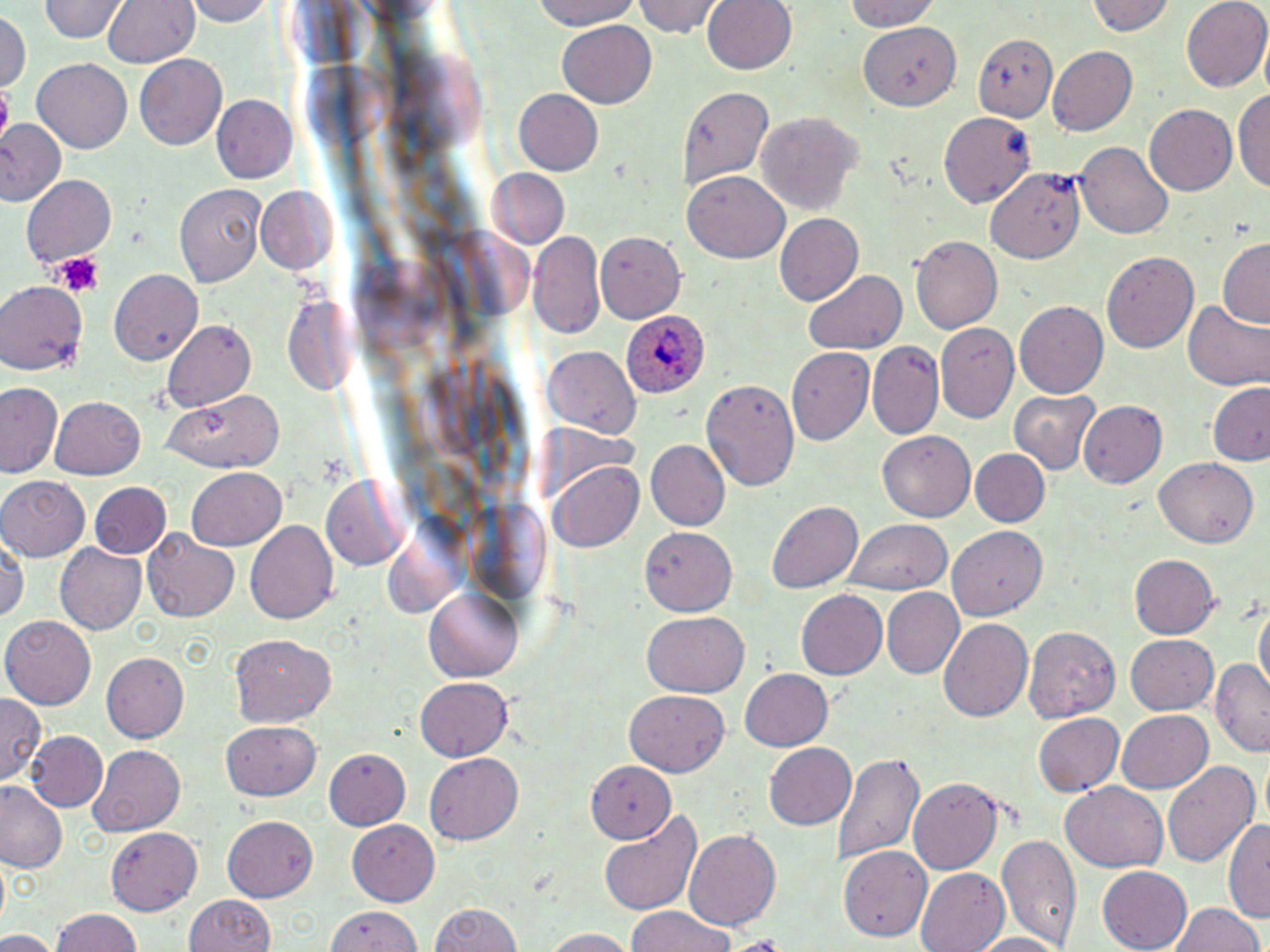

Summary:
  - Coordinate format: approximate bounding boxes as named x1/y1/x2/y2 corners in pixels
  - Platelet locations: (x1=0, y1=88, x2=12, y2=133), (x1=50, y1=252, x2=106, y2=298)
  - Uninfected red blood cell locations: (x1=40, y1=0, x2=127, y2=44), (x1=102, y1=0, x2=199, y2=70), (x1=188, y1=0, x2=274, y2=26), (x1=528, y1=0, x2=646, y2=29), (x1=634, y1=0, x2=725, y2=39), (x1=703, y1=0, x2=798, y2=75), (x1=840, y1=0, x2=943, y2=32), (x1=1090, y1=0, x2=1176, y2=38), (x1=1182, y1=0, x2=1270, y2=93), (x1=0, y1=13, x2=29, y2=90), (x1=558, y1=19, x2=657, y2=108), (x1=859, y1=19, x2=967, y2=110), (x1=974, y1=33, x2=1057, y2=120), (x1=1046, y1=46, x2=1136, y2=137), (x1=134, y1=55, x2=227, y2=150), (x1=33, y1=58, x2=132, y2=154), (x1=1234, y1=83, x2=1270, y2=195), (x1=676, y1=85, x2=772, y2=193), (x1=514, y1=89, x2=605, y2=176), (x1=213, y1=95, x2=299, y2=183), (x1=1197, y1=96, x2=1269, y2=192), (x1=1146, y1=104, x2=1238, y2=197), (x1=937, y1=109, x2=1036, y2=208), (x1=757, y1=112, x2=862, y2=215), (x1=0, y1=119, x2=65, y2=205), (x1=1076, y1=142, x2=1174, y2=240), (x1=486, y1=168, x2=570, y2=252), (x1=989, y1=168, x2=1086, y2=263), (x1=683, y1=171, x2=789, y2=264), (x1=21, y1=175, x2=117, y2=267), (x1=175, y1=182, x2=267, y2=291), (x1=254, y1=187, x2=340, y2=276), (x1=773, y1=213, x2=864, y2=307), (x1=527, y1=232, x2=606, y2=339), (x1=598, y1=232, x2=684, y2=321), (x1=911, y1=236, x2=1002, y2=334), (x1=1218, y1=238, x2=1270, y2=327), (x1=1102, y1=248, x2=1198, y2=352), (x1=107, y1=269, x2=201, y2=365), (x1=804, y1=270, x2=907, y2=358), (x1=0, y1=281, x2=85, y2=373), (x1=1184, y1=300, x2=1269, y2=390), (x1=1015, y1=301, x2=1108, y2=397), (x1=162, y1=321, x2=256, y2=410), (x1=936, y1=321, x2=1018, y2=423), (x1=867, y1=342, x2=942, y2=438), (x1=787, y1=344, x2=874, y2=444), (x1=543, y1=347, x2=640, y2=439), (x1=700, y1=379, x2=799, y2=490), (x1=1209, y1=380, x2=1270, y2=466), (x1=0, y1=383, x2=62, y2=478), (x1=163, y1=389, x2=284, y2=473), (x1=1010, y1=389, x2=1101, y2=474), (x1=50, y1=396, x2=146, y2=481), (x1=1076, y1=400, x2=1165, y2=490), (x1=877, y1=430, x2=976, y2=521), (x1=645, y1=441, x2=731, y2=531), (x1=968, y1=448, x2=1051, y2=529), (x1=547, y1=458, x2=645, y2=556), (x1=1155, y1=459, x2=1258, y2=546), (x1=187, y1=468, x2=285, y2=550), (x1=0, y1=475, x2=88, y2=560), (x1=320, y1=476, x2=408, y2=571), (x1=89, y1=482, x2=172, y2=560), (x1=767, y1=501, x2=864, y2=594), (x1=245, y1=518, x2=338, y2=624), (x1=843, y1=518, x2=953, y2=597), (x1=641, y1=525, x2=737, y2=613), (x1=947, y1=525, x2=1045, y2=620), (x1=143, y1=528, x2=242, y2=622), (x1=1, y1=541, x2=26, y2=626), (x1=55, y1=542, x2=146, y2=634), (x1=1127, y1=553, x2=1218, y2=640), (x1=423, y1=584, x2=525, y2=684), (x1=881, y1=587, x2=965, y2=678), (x1=797, y1=591, x2=888, y2=680), (x1=1253, y1=600, x2=1268, y2=699), (x1=641, y1=612, x2=748, y2=696), (x1=3, y1=615, x2=98, y2=708), (x1=938, y1=616, x2=1032, y2=721), (x1=1024, y1=626, x2=1120, y2=721), (x1=1124, y1=634, x2=1219, y2=714), (x1=227, y1=635, x2=335, y2=729), (x1=102, y1=652, x2=189, y2=743), (x1=1212, y1=660, x2=1269, y2=755), (x1=738, y1=668, x2=833, y2=752), (x1=417, y1=675, x2=513, y2=760), (x1=626, y1=689, x2=728, y2=775), (x1=0, y1=696, x2=45, y2=785), (x1=1117, y1=708, x2=1214, y2=793), (x1=1032, y1=713, x2=1124, y2=797), (x1=221, y1=721, x2=321, y2=801), (x1=26, y1=732, x2=110, y2=813), (x1=766, y1=742, x2=857, y2=831), (x1=88, y1=745, x2=184, y2=836), (x1=326, y1=747, x2=410, y2=829), (x1=832, y1=749, x2=924, y2=870), (x1=425, y1=752, x2=525, y2=845), (x1=1160, y1=759, x2=1259, y2=869), (x1=584, y1=761, x2=674, y2=844), (x1=907, y1=778, x2=1005, y2=875), (x1=1061, y1=782, x2=1170, y2=873), (x1=0, y1=784, x2=66, y2=872), (x1=597, y1=810, x2=703, y2=916), (x1=1225, y1=815, x2=1270, y2=924), (x1=222, y1=817, x2=318, y2=901), (x1=348, y1=820, x2=438, y2=903), (x1=105, y1=826, x2=202, y2=913), (x1=683, y1=829, x2=781, y2=930), (x1=995, y1=832, x2=1080, y2=950), (x1=841, y1=846, x2=931, y2=940), (x1=1097, y1=867, x2=1193, y2=951), (x1=914, y1=868, x2=1009, y2=952), (x1=179, y1=893, x2=281, y2=952), (x1=428, y1=900, x2=528, y2=952), (x1=1170, y1=902, x2=1262, y2=952), (x1=49, y1=907, x2=148, y2=952), (x1=627, y1=907, x2=735, y2=952), (x1=329, y1=908, x2=424, y2=952), (x1=539, y1=928, x2=639, y2=951), (x1=0, y1=930, x2=56, y2=952), (x1=971, y1=933, x2=1070, y2=952), (x1=730, y1=938, x2=789, y2=949)
  - Plasmodium ovale-infected red blood cell locations: (x1=620, y1=311, x2=712, y2=401)
  - Slide-level diagnosis: Plasmodium ovale
  - Field of view: single
  - Preparation: thin blood smear
  - Magnification: 1000x
  - Modality: light microscopy
  - Stain: May-Grünwald-Giemsa
  - Image size: 1270×952 pixels